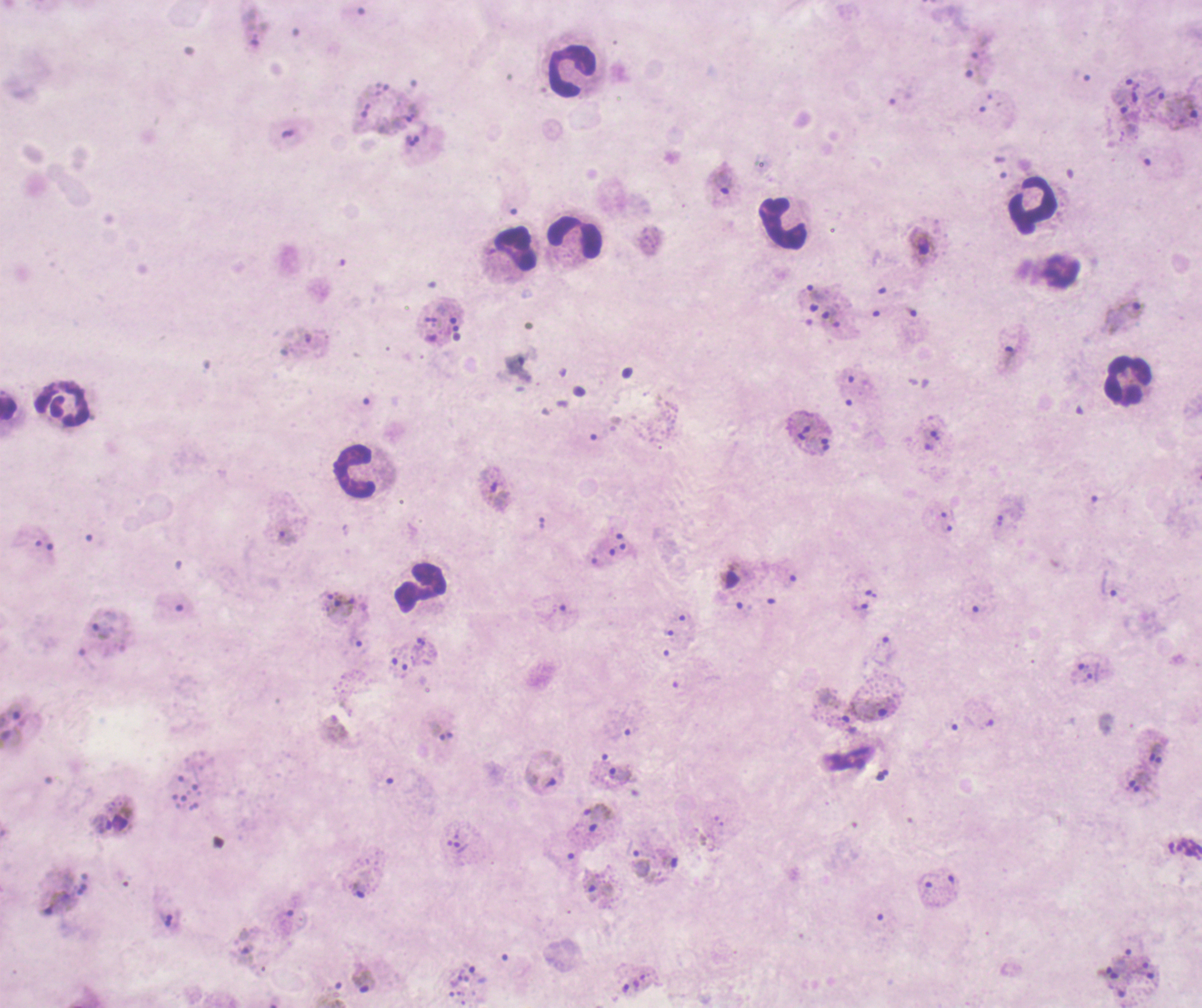 Approximate centers as (x, y) in pixels. Trophozoite locations: (974, 72), (1154, 92), (1189, 107), (410, 117), (723, 180), (815, 292), (1132, 310), (829, 313), (1008, 357), (935, 435), (498, 494), (1000, 521), (1109, 585), (862, 611), (102, 624), (1085, 678), (876, 707), (14, 712), (12, 738), (1156, 754), (622, 775), (542, 785), (598, 812), (460, 846), (640, 863), (357, 890), (57, 902), (1140, 967), (1147, 975), (365, 979), (625, 988). Leukocyte locations: (570, 72), (1032, 203), (782, 222), (575, 237), (516, 249), (1126, 383), (8, 409), (354, 470), (421, 587). Gametocyte locations: (921, 245), (730, 574), (121, 816). Life-cycle stages observed: trophozoite, gametocyte. Image is 1202×1008 pixels. Result: positive for Plasmodium parasites. 100x magnification. Single field of view. Coloration quality: bad. Thick blood smear. Background quality: poor. Romanowsky-stained preparation. Previously used in an actual diagnosis.